Classify this cell by malaria status.
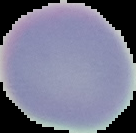
It is uninfected.

Image is 136×133 pixels. The area outside the segmented cell region is set to black. From a thin blood film.